Report the malaria status of this cell.
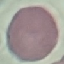

It is uninfected.

stain = Giemsa
capture = smartphone camera at the microscope eyepiece
image type = automatically extracted cell patch, resized to 64 × 64 pixels
preparation = thin blood film